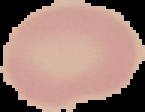

malaria status = uninfected
image type = cell region segmented out of the field of view; surrounding area masked to black
image size = 145×112 pixels
preparation = thin blood smear